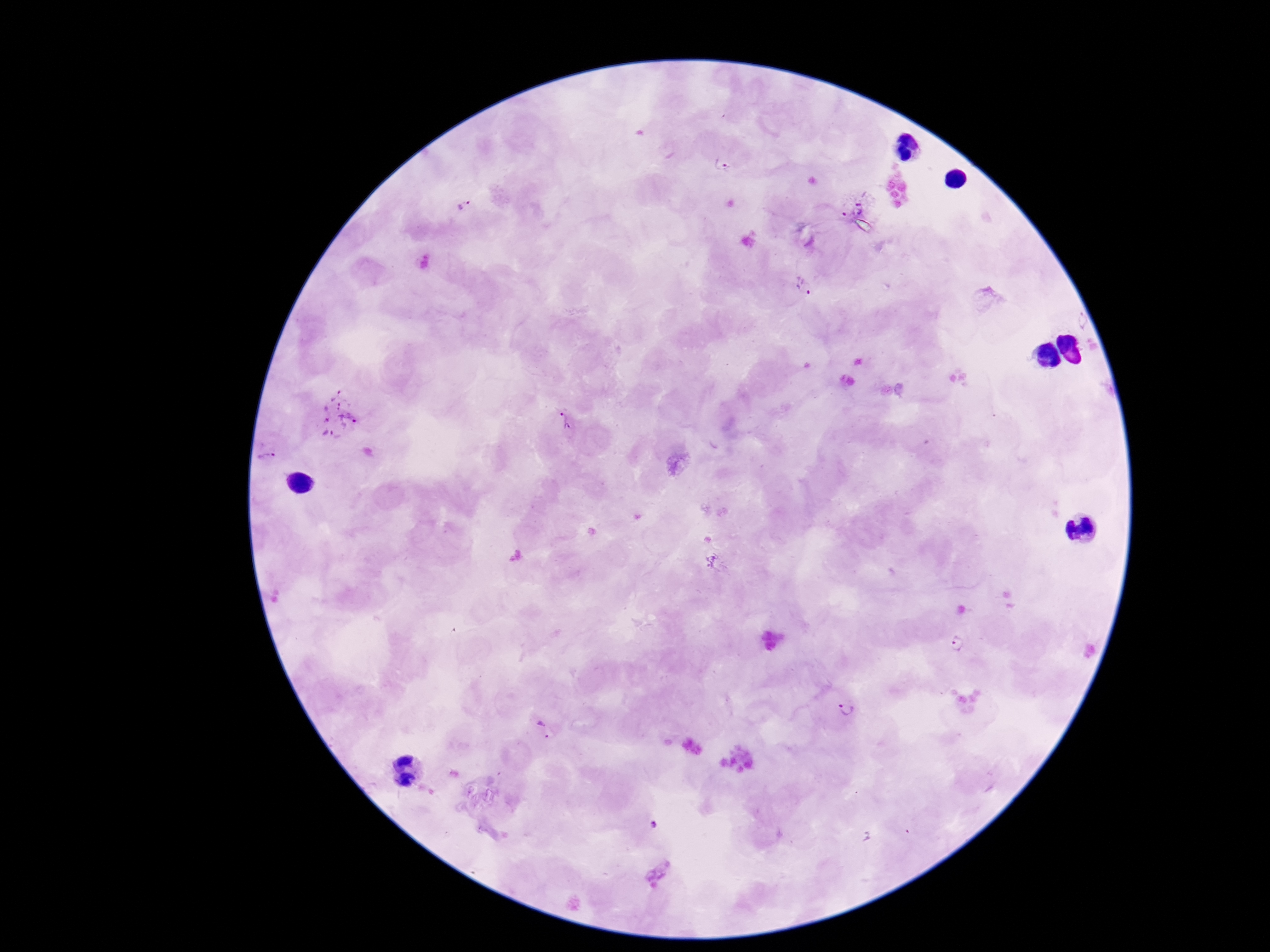

Approximate object centers, in pixels from the top-left corner.
Summary:
  - Plasmodium parasite locations: (x=724, y=166), (x=855, y=205), (x=464, y=206), (x=805, y=289), (x=336, y=415), (x=564, y=420), (x=269, y=456), (x=958, y=643), (x=847, y=709), (x=544, y=729), (x=653, y=825)
  - Capture: smartphone camera through the microscope eyepiece
  - Patient malaria status: infected
  - Magnification: 100x
  - Preparation: thick peripheral-blood smear
  - Field of view: single
  - Stain: Giemsa
  - Image size: 1270×952 pixels